Identify the parasite.
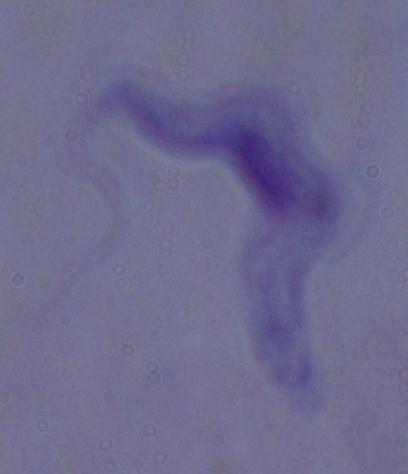
A trypanosome.

magnification = 1000x
modality = photomicrograph